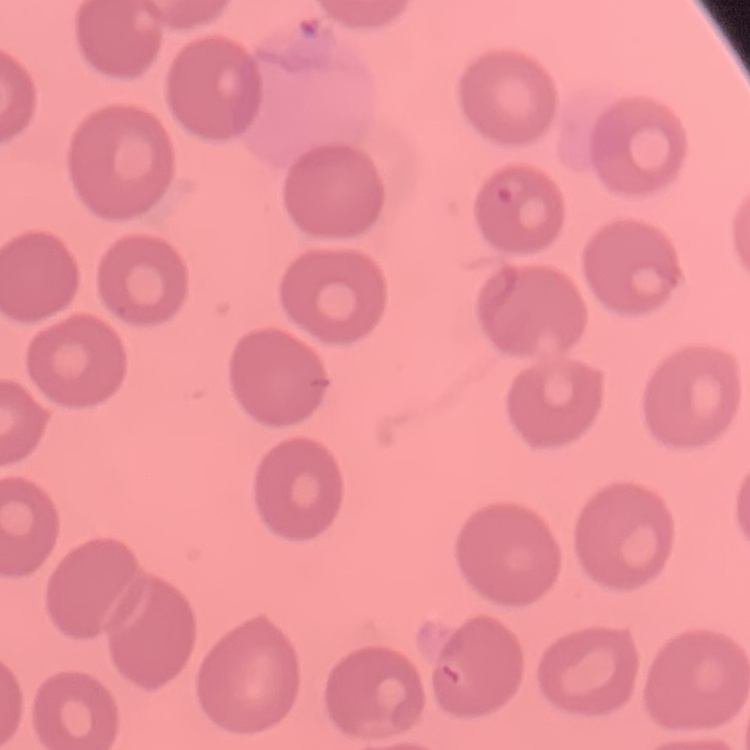 The red blood cells exhibit no rouleaux formation. Thin peripheral smear. Square crop of a larger photomicrograph. Field's or Giemsa stain.